Locate every Plasmodium parasite and every leukocyte.
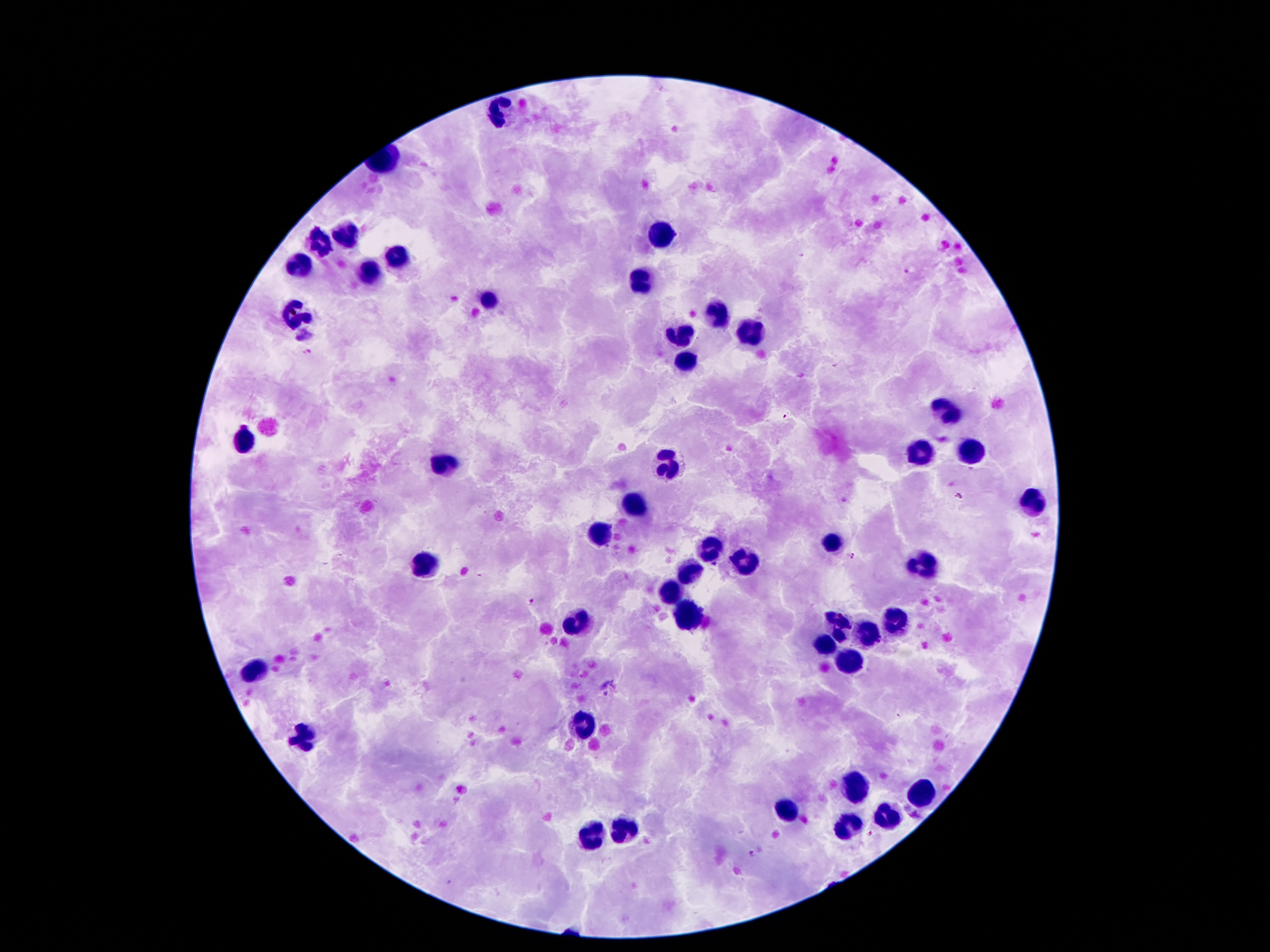

Approximate centers as (x, y) in pixels.
Plasmodium parasites: (905, 272), (308, 351), (785, 417), (958, 496), (851, 557), (714, 565), (527, 601), (898, 716), (751, 855).
Leukocytes: (503, 113), (661, 239), (343, 240), (319, 244), (403, 253), (301, 269), (371, 273), (641, 285), (491, 301), (715, 315), (299, 316), (747, 332), (681, 336), (685, 357), (945, 413), (245, 439), (971, 454), (919, 455), (667, 465), (443, 467), (1029, 504), (635, 505), (605, 534), (831, 544), (709, 551), (425, 561), (745, 561), (921, 563), (689, 569), (673, 590), (685, 614), (891, 620), (837, 623), (575, 624), (869, 630), (823, 645), (849, 660), (255, 671), (583, 724), (301, 735), (855, 789), (921, 795), (783, 809), (887, 817), (847, 827), (623, 830), (591, 835).

Summary:
  - Preparation: thick peripheral-blood smear
  - Patient malaria status: positive for Plasmodium falciparum
  - Image size: 1270×952 pixels
  - Stain: Giemsa
  - Magnification: 100x
  - Field of view: single
  - Capture: smartphone camera through the microscope eyepiece